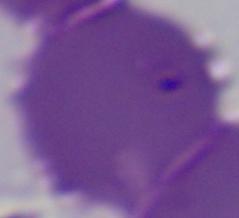
Summary:
  - Magnification: 1000x
  - Modality: micrograph
  - Identification: Babesia